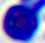

Summary:
  - Identification: leukocyte
  - Magnification: 400x
  - Modality: photomicrograph